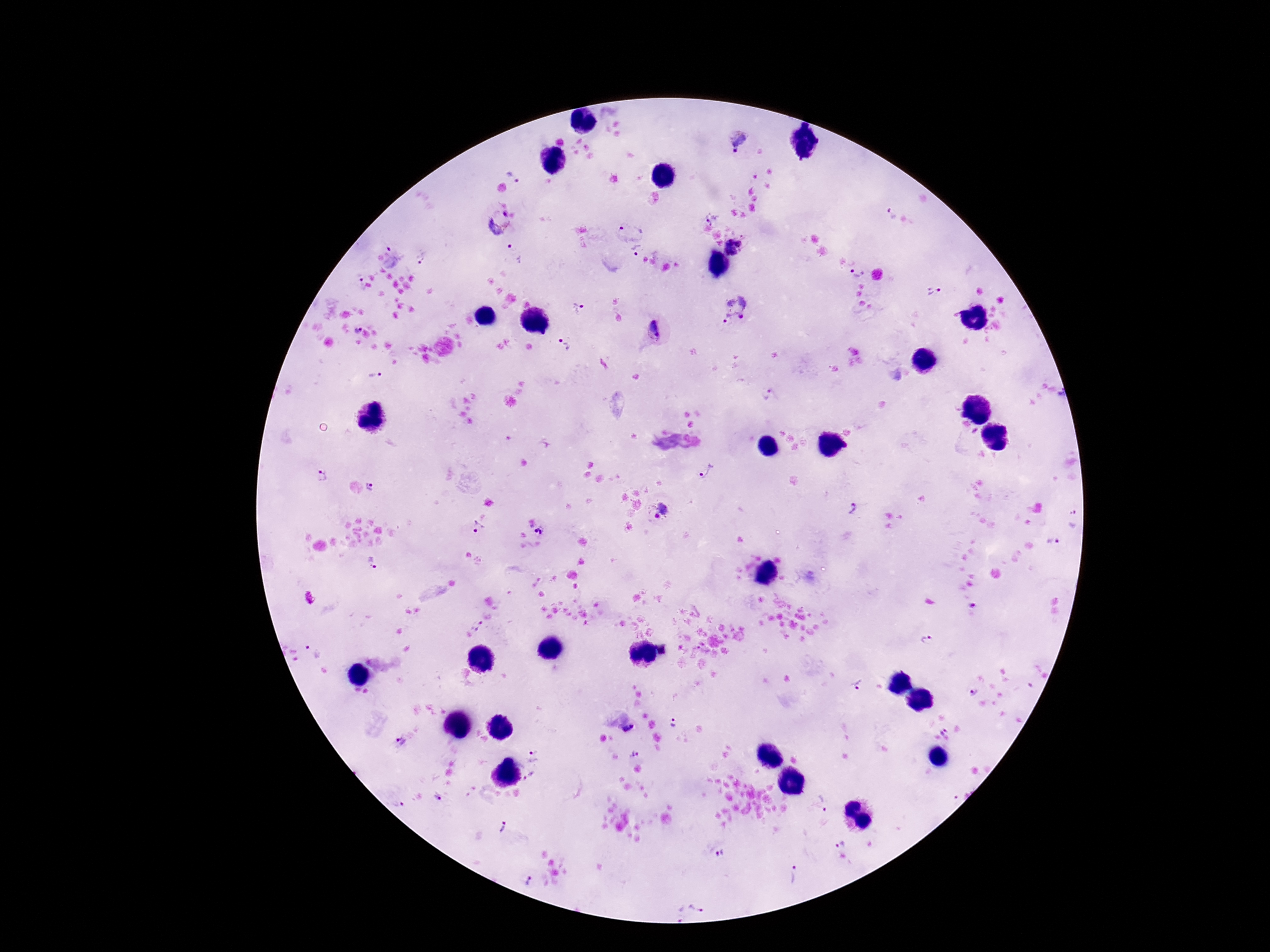

field of view = one from this slide
patient malaria status = positive
magnification = 100x
Plasmodium parasite locations = approximate centers as [x, y] in pixels: [736, 140], [514, 176], [891, 212], [499, 222], [709, 223], [630, 227], [729, 241], [739, 243], [392, 249], [516, 250], [637, 251], [732, 253], [423, 258], [858, 273], [359, 281], [933, 291], [579, 308], [733, 310], [354, 329], [654, 331], [564, 344], [375, 375], [769, 395], [708, 472], [323, 476], [372, 486], [851, 507], [656, 510], [477, 527], [539, 531], [1052, 542], [373, 562], [972, 609], [478, 625], [926, 641], [315, 650], [859, 685], [972, 693], [673, 722], [629, 729], [945, 734], [399, 741], [535, 756], [530, 777], [437, 798], [397, 803], [824, 804], [503, 829], [840, 843], [721, 855], [795, 877], [530, 879], [698, 906], [679, 913]
image size = 1270×952 pixels
preparation = thick blood smear
capture = smartphone camera through the microscope eyepiece
stain = Giemsa